Locate every Plasmodium parasite.
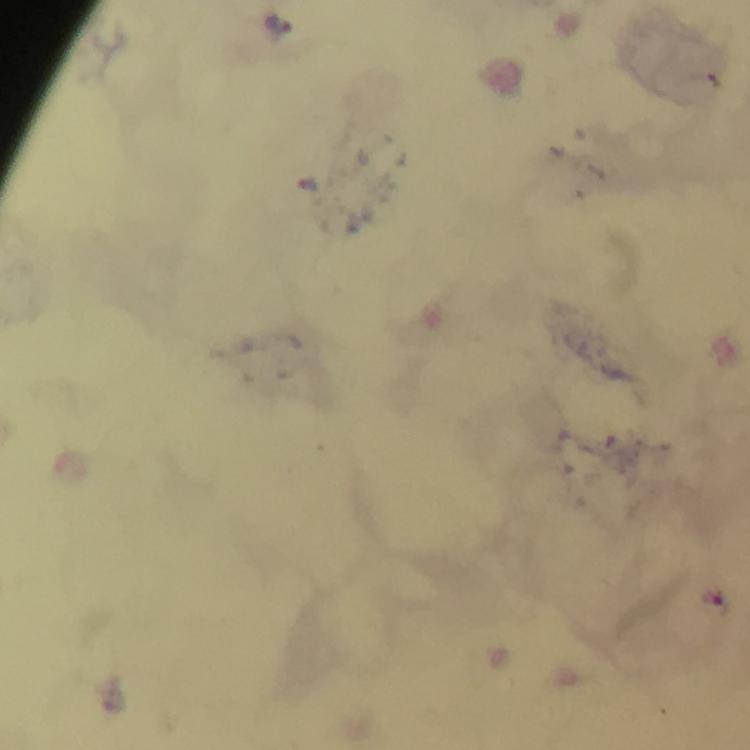
Approximate centers as {x, y} in pixels.
Plasmodium parasites: {279, 22}.

From a malaria diagnostic workup. Cropped region of a single field of view. Image is 750×750 pixels. Giemsa stain. Immersion oil was used. Thick blood smear. At 100x magnification. Smartphone photograph taken through a microscope.